Give the position of each P. falciparum parasite with its life-cycle stage, each leukocyte, and any debris.
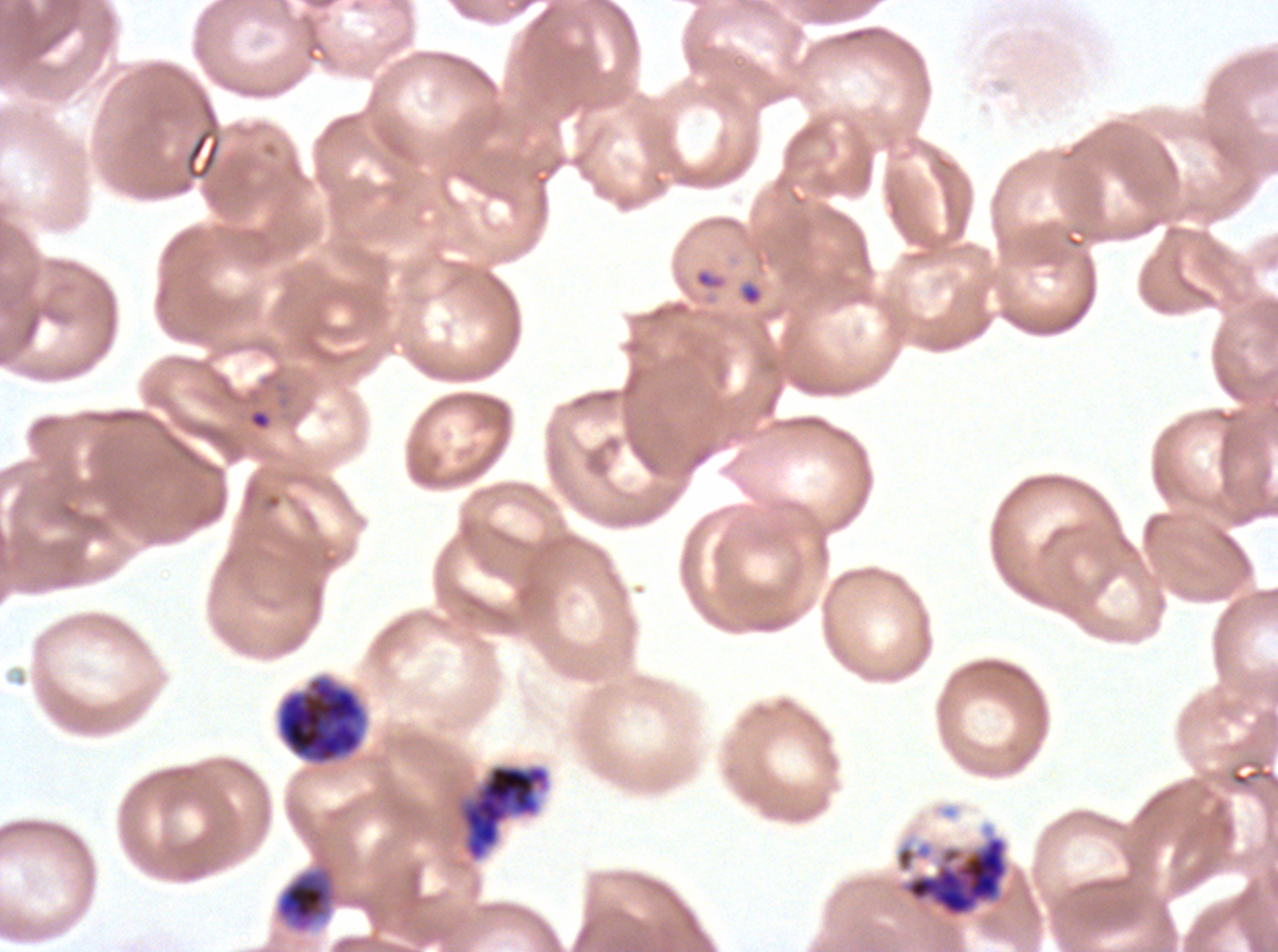

Approximate bounding boxes as [x1, y1, x2, y2] in pixels.
Rings: [247, 408, 273, 432].
Early schizonts: [276, 676, 366, 764], [461, 764, 549, 860], [275, 863, 339, 934].
Segmenters: [899, 834, 1011, 920].
Debris: [693, 266, 729, 292].
No late-ring/early-trophozoite forms, mid trophozoites, late trophozoites, late schizonts, gametocytes, or leukocytes observed.

preparation = thin blood film
stain = Giemsa
specimen = P. falciparum cultured ex vivo for 24 to 48 hours, from a patient in The Gambia
life-cycle stages observed = ring, early schizont, segmenter
image size = 1278×952 pixels
field of view = one sub-image of a larger composite